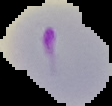

Summary:
  - Image size: 112×106 pixels
  - Result: Plasmodium parasites identified
  - Preparation: thin blood smear
  - Image type: cell region segmented out of the field of view; surrounding area masked to black